Point out each leukocyte.
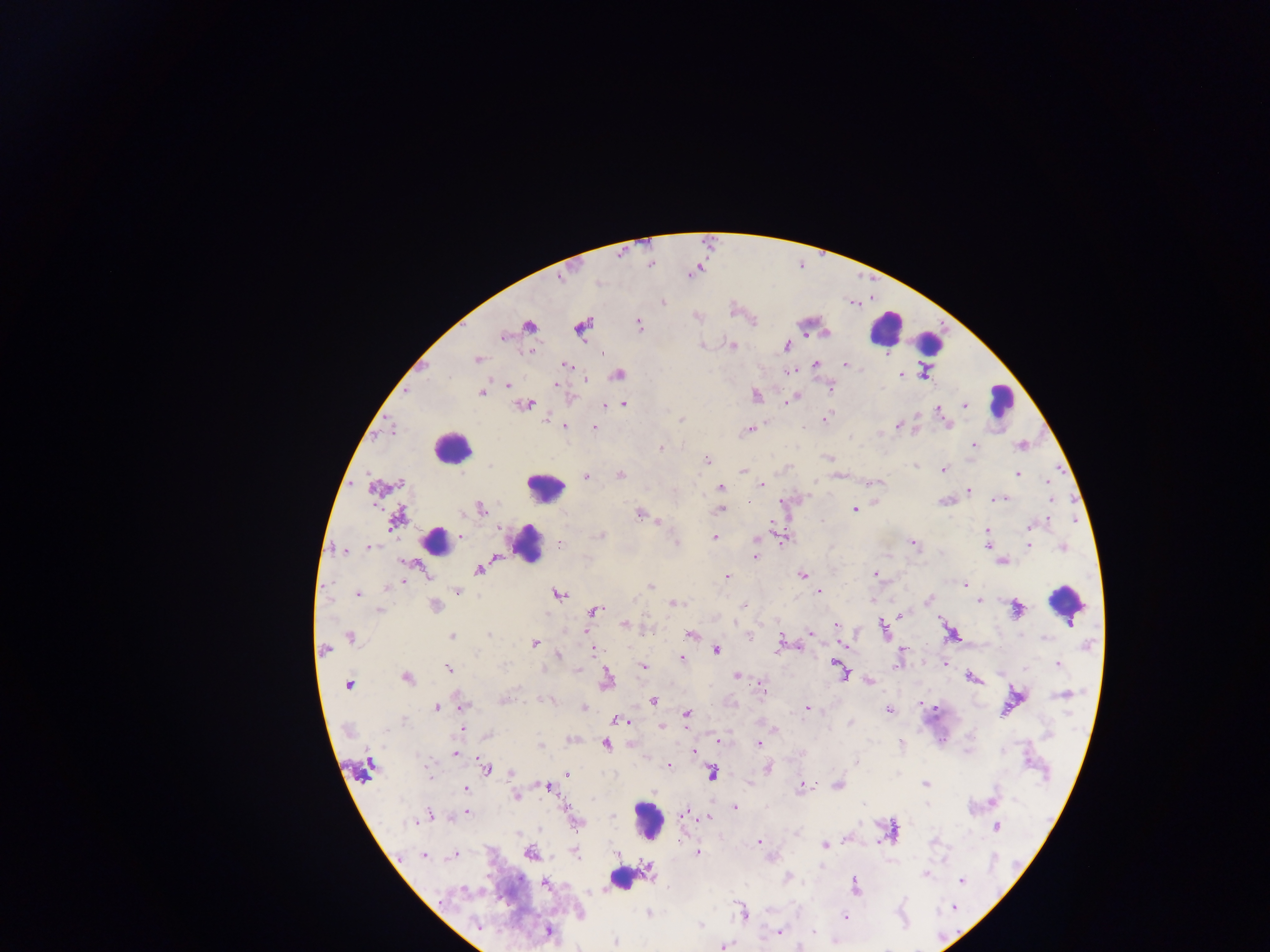

Approximate centers as [x, y] in pixels.
Leukocytes: [885, 328], [931, 347], [1001, 400], [451, 447], [545, 487], [433, 539], [528, 544], [1066, 603], [648, 820], [624, 877].

Malaria parasite locations: [664, 302], [638, 324], [528, 326], [582, 327], [503, 336], [733, 346], [786, 347], [530, 351], [477, 359], [815, 363], [846, 364], [566, 365], [788, 371], [618, 374], [900, 374], [585, 379], [507, 385], [555, 385], [830, 387], [481, 393], [756, 395], [790, 399], [623, 404], [525, 405], [605, 405], [965, 405], [941, 413], [827, 417], [681, 420], [898, 426], [565, 427], [594, 427], [805, 427], [749, 430], [973, 445], [1020, 446], [661, 448], [828, 458], [707, 460], [916, 465], [943, 470], [743, 471], [1017, 474], [620, 475], [586, 478], [1047, 482], [399, 483], [762, 484], [720, 487], [968, 490], [999, 499], [1050, 499], [480, 509], [854, 509], [720, 510], [639, 514], [395, 520], [1029, 526], [498, 529], [987, 531], [460, 536], [602, 536], [715, 537], [758, 539], [676, 542], [913, 543], [559, 544], [1029, 545], [987, 546], [369, 547], [1063, 547], [344, 551], [756, 557], [1002, 561], [479, 569], [802, 574], [875, 574], [727, 577], [403, 583], [965, 584], [388, 587], [650, 587], [458, 590], [820, 592], [358, 594], [559, 594], [928, 600], [980, 601], [676, 603], [744, 605], [435, 606], [1016, 609], [379, 610], [594, 611], [902, 614], [624, 624], [836, 625], [883, 627], [585, 633], [810, 633], [691, 634], [951, 634], [489, 635], [750, 635], [452, 636], [351, 637], [780, 643], [535, 644], [844, 645], [325, 649], [902, 649], [716, 650], [595, 651], [559, 655], [681, 658], [945, 664], [835, 665], [896, 665], [1058, 665], [502, 666], [644, 666], [448, 668], [576, 670], [842, 672], [737, 676], [971, 678], [408, 679], [607, 679], [869, 682], [349, 685], [761, 687], [1065, 695], [504, 699], [549, 700], [652, 701], [462, 706], [584, 707], [437, 708], [935, 708], [807, 709], [889, 710], [687, 714], [403, 720], [619, 721], [850, 723], [663, 726], [775, 730], [488, 735], [719, 741], [759, 744], [901, 744], [606, 745], [540, 746], [693, 751], [455, 753], [857, 763], [370, 765], [668, 766], [767, 768], [486, 769], [512, 773], [712, 773], [567, 774], [924, 784], [806, 785], [838, 785], [547, 787], [799, 787], [466, 790], [516, 797], [994, 800], [863, 805], [927, 805], [735, 808], [686, 810], [466, 812], [430, 814], [612, 816], [708, 818], [412, 822], [577, 822], [997, 827], [519, 833], [758, 842], [825, 845], [576, 853], [698, 853], [531, 854], [617, 854], [423, 855], [454, 856], [648, 870], [925, 874], [789, 878], [961, 881], [546, 883], [855, 886], [464, 889], [954, 907], [648, 913], [743, 913], [845, 917], [700, 925], [477, 926], [548, 932], [779, 932], [813, 932], [616, 942], [725, 946], [799, 947]. Thick blood film. Collected in Ghana. Photographed through a microscope with a mobile-phone camera. One field of view. Image is 1270×952 pixels.